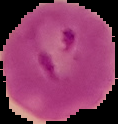

image_size: 118×124 pixels
result: Plasmodium parasites detected
image_type: segmented cell region with the area outside set to black
preparation: thin blood film